Point out each malaria parasite.
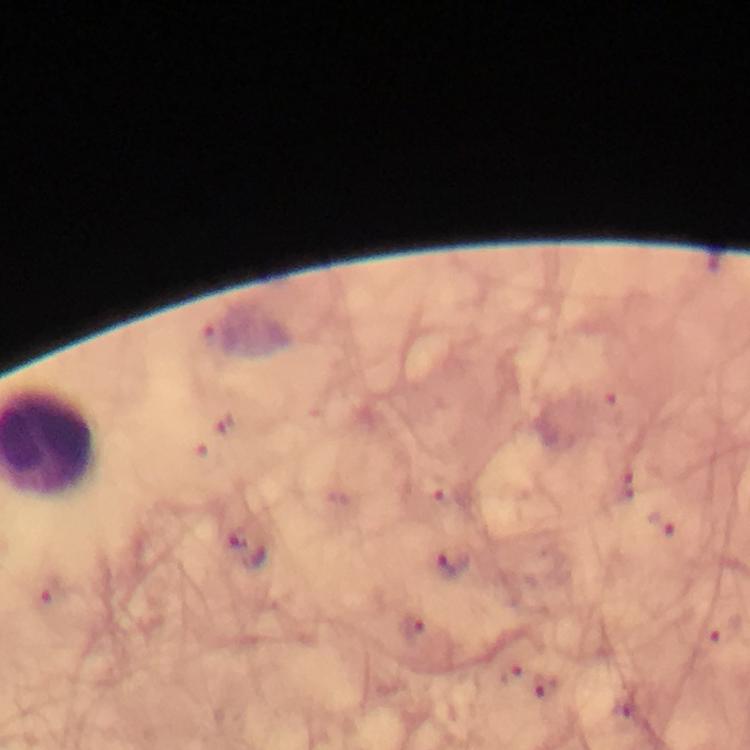

Approximate object centers, in pixels from the top-left corner.
Malaria parasites: (x=660, y=524), (x=235, y=535), (x=453, y=562), (x=412, y=628), (x=544, y=688).

context = from a malaria diagnostic workup
image size = 750×750 pixels
cropped from = one field of view
preparation = thick blood film
stain = Giemsa
capture = smartphone mounted on the microscope
magnification = 100x
immersion oil = applied